State the preparation type.
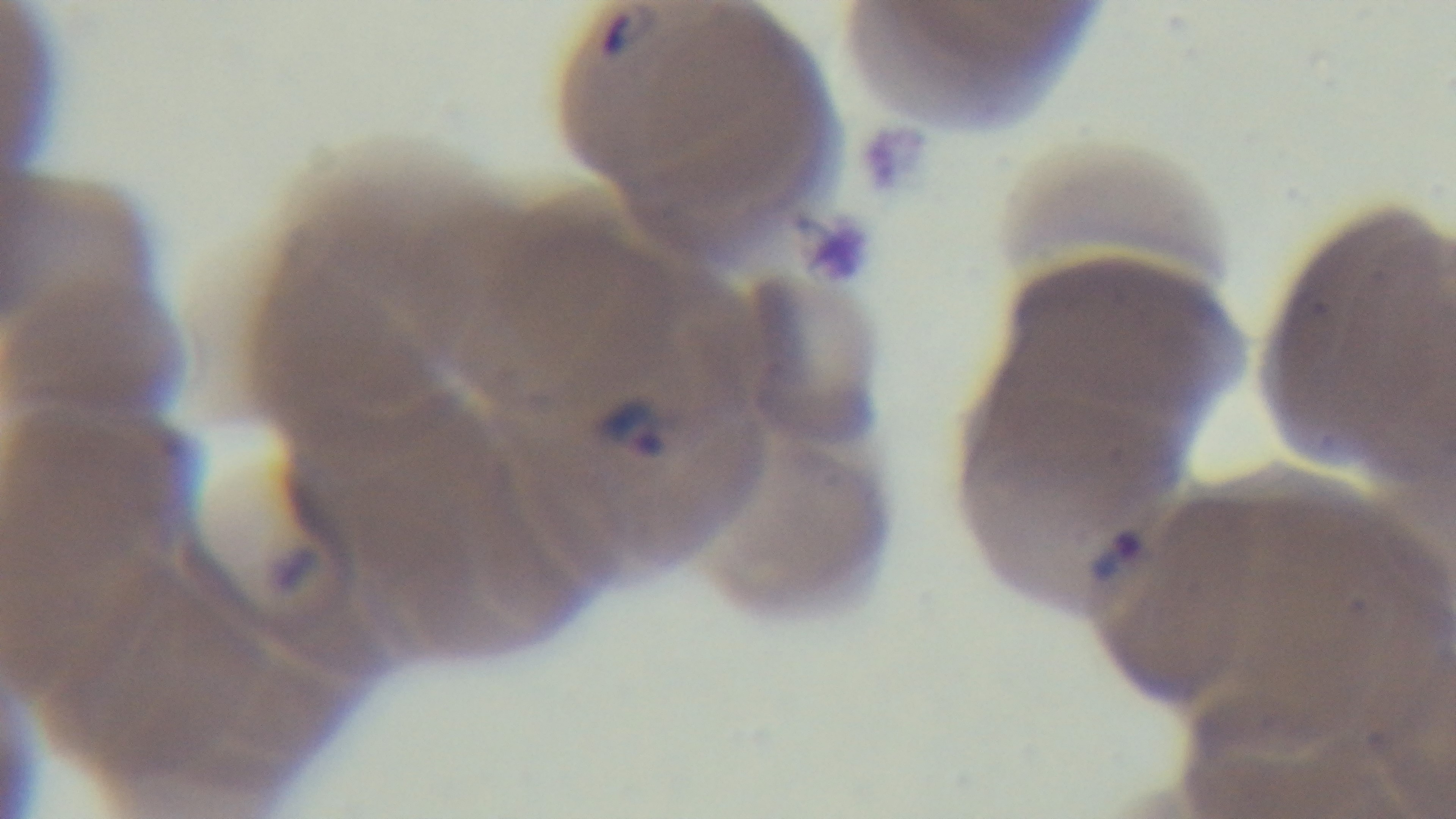
Thin.

{
  "modality": "light microscopy",
  "objective": "100x oil immersion",
  "malaria_status": "infected",
  "field_of_view": "single",
  "capture": "mounted 4K digital camera",
  "stain": "Giemsa"
}